Report the malaria status of this cell.
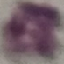
It is uninfected.

capture = smartphone camera at the microscope eyepiece
stain = Giemsa
preparation = thin blood film
image type = automatically extracted cell patch, resized to 64 × 64 pixels